Evaluate for malaria.
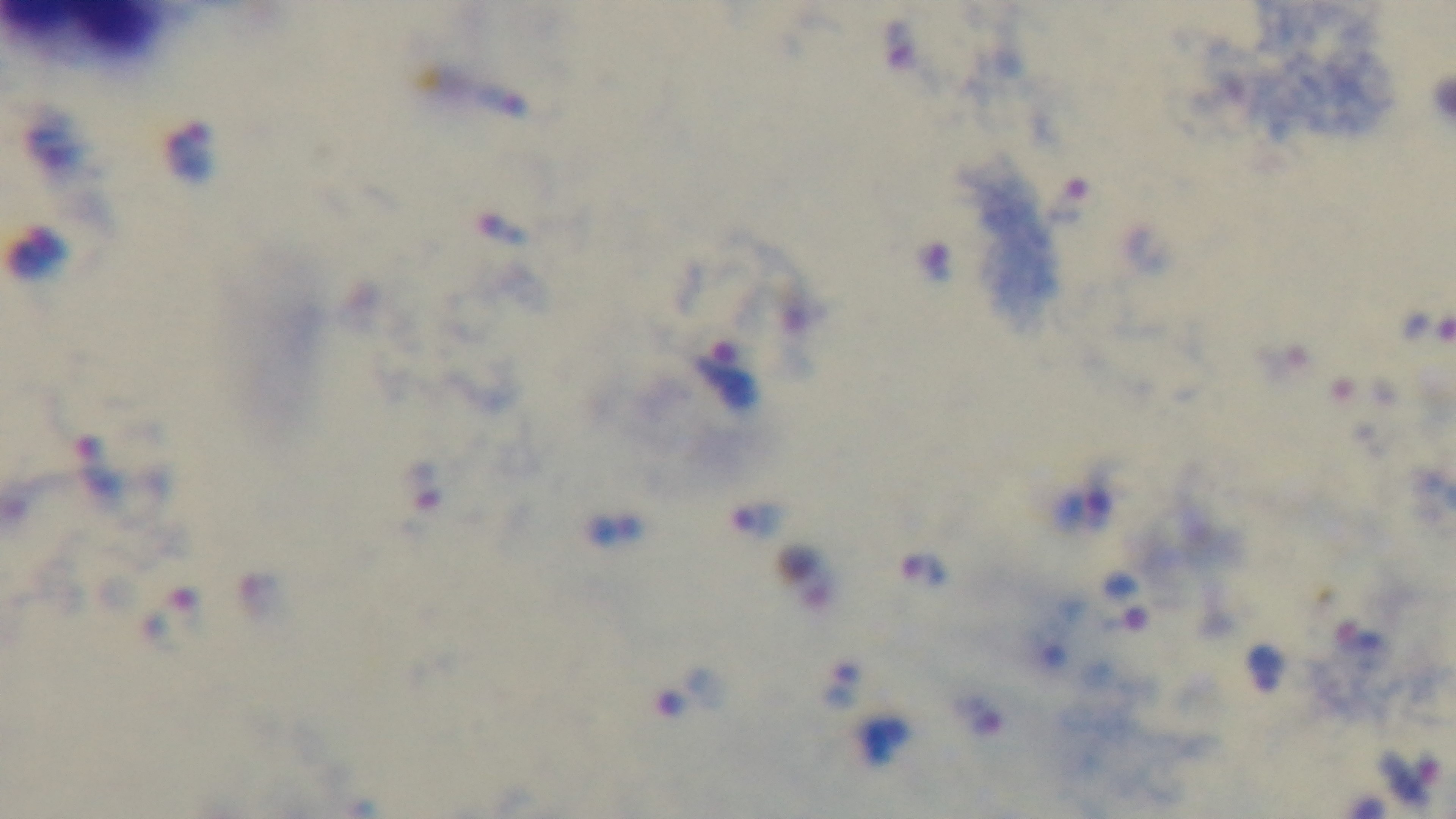

It is infected.

Summary:
  - Modality: light microscopy
  - Stain: Giemsa
  - Objective: 100x oil immersion
  - Capture: mounted 4K digital camera
  - Field of view: single
  - Preparation: thick